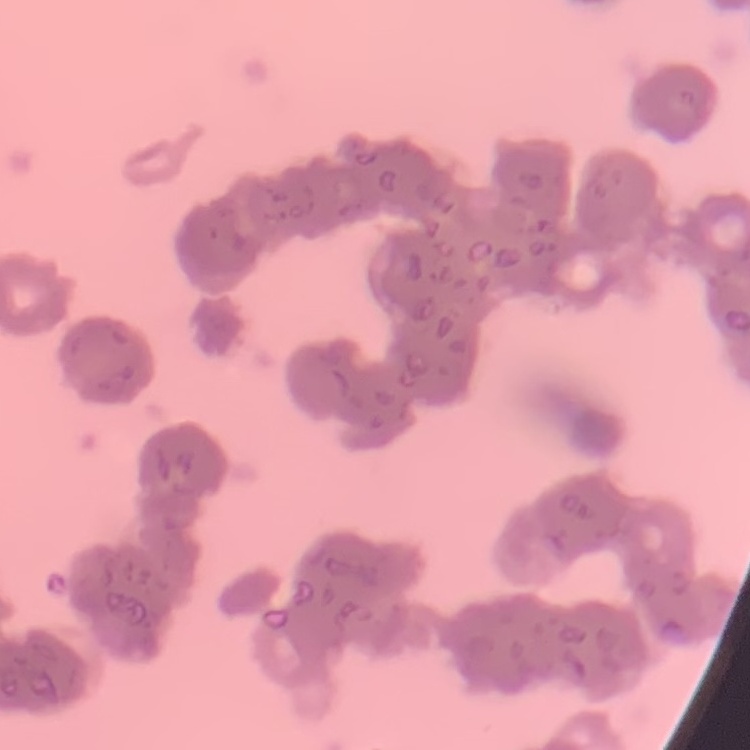
Summary:
  - Erythrocyte morphology: rouleaux formation
  - Preparation: thin peripheral smear
  - Image type: square crop of a larger photomicrograph
  - Stain: Field's or Giemsa